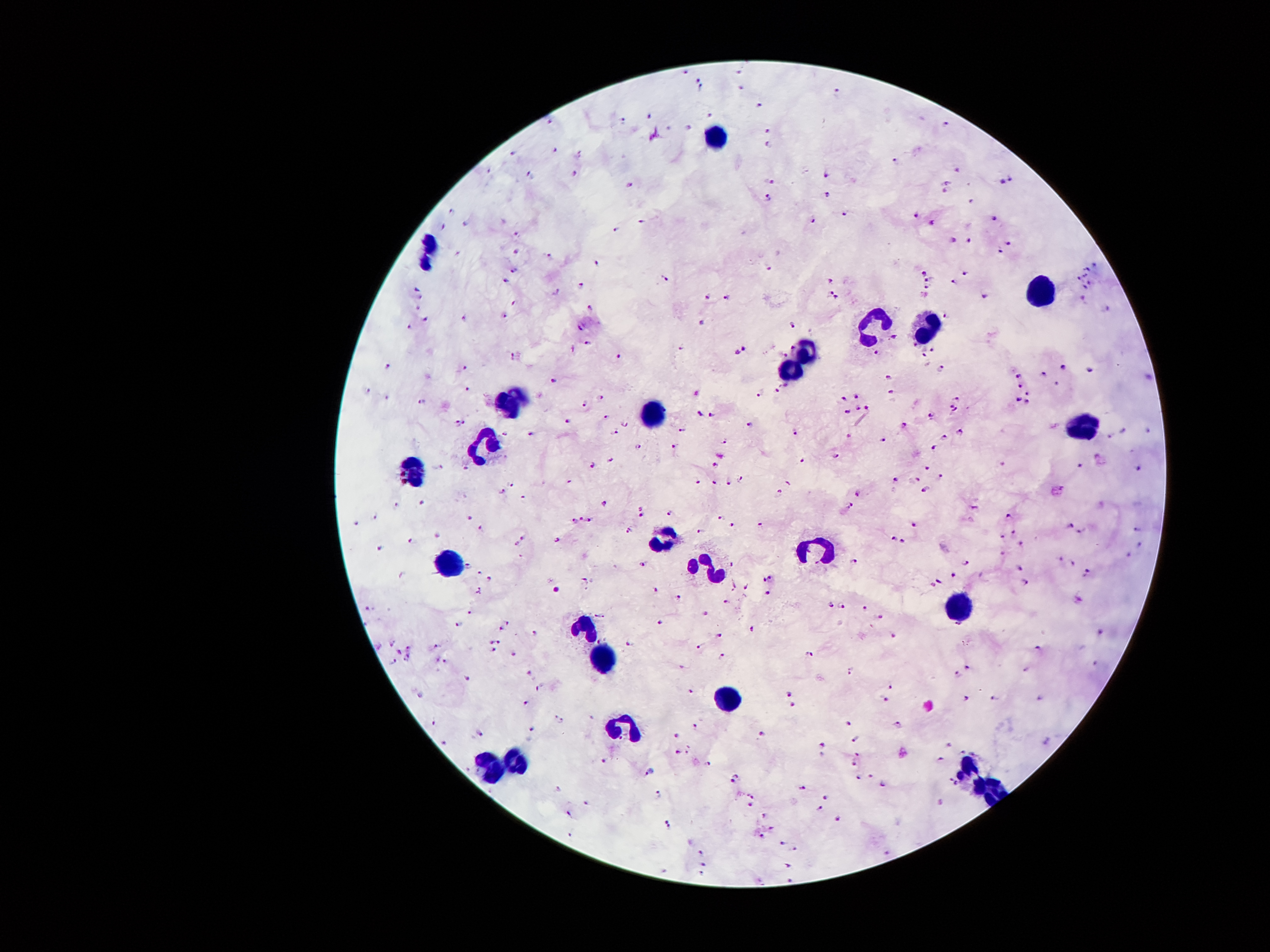

{
  "stain": "Giemsa",
  "leukocyte_locations": "approximate object centers, in pixels from the top-left corner: (x=714, y=135), (x=425, y=253), (x=1038, y=293), (x=870, y=328), (x=928, y=329), (x=801, y=356), (x=788, y=369), (x=509, y=402), (x=649, y=414), (x=1088, y=427), (x=486, y=446), (x=414, y=471), (x=666, y=545), (x=807, y=551), (x=448, y=566), (x=708, y=571), (x=956, y=610), (x=586, y=625), (x=605, y=659), (x=731, y=699), (x=628, y=726), (x=511, y=764), (x=486, y=766), (x=966, y=766), (x=989, y=793)",
  "image_size": "1270×952 pixels",
  "preparation": "thick blood smear",
  "field_of_view": "single",
  "magnification": "100x",
  "plasmodium_parasite_locations": "approximate object centers, in pixels from the top-left corner: (x=686, y=73), (x=739, y=73), (x=698, y=78), (x=701, y=89), (x=741, y=89), (x=835, y=93), (x=757, y=105), (x=708, y=113), (x=649, y=118), (x=550, y=122), (x=621, y=123), (x=945, y=125), (x=688, y=129), (x=767, y=131), (x=770, y=146), (x=556, y=150), (x=514, y=154), (x=579, y=155), (x=897, y=162), (x=574, y=174), (x=826, y=174), (x=531, y=175), (x=1009, y=178), (x=1002, y=181), (x=768, y=182), (x=946, y=182), (x=629, y=185), (x=946, y=192), (x=827, y=195), (x=769, y=199), (x=971, y=200), (x=451, y=212), (x=844, y=213), (x=917, y=213), (x=994, y=218), (x=814, y=221), (x=641, y=222), (x=465, y=223), (x=933, y=224), (x=443, y=227), (x=617, y=229), (x=516, y=235), (x=953, y=240), (x=968, y=242), (x=1009, y=243), (x=999, y=250), (x=517, y=253), (x=457, y=254), (x=548, y=257), (x=598, y=264), (x=1093, y=266), (x=767, y=268), (x=1086, y=270), (x=513, y=272), (x=923, y=273), (x=963, y=273), (x=1085, y=277), (x=664, y=278), (x=833, y=278), (x=1078, y=279), (x=506, y=280), (x=926, y=280), (x=953, y=282), (x=580, y=284), (x=1088, y=284), (x=928, y=287), (x=1083, y=288), (x=554, y=292), (x=829, y=293), (x=987, y=293), (x=707, y=296), (x=420, y=297), (x=836, y=297), (x=1083, y=297), (x=726, y=298), (x=510, y=303), (x=590, y=307), (x=417, y=308), (x=1105, y=310), (x=945, y=314), (x=503, y=316), (x=424, y=317), (x=465, y=319), (x=701, y=322), (x=794, y=324), (x=581, y=326), (x=408, y=327), (x=896, y=336), (x=588, y=343), (x=915, y=347), (x=933, y=348), (x=681, y=349), (x=745, y=350), (x=735, y=352), (x=783, y=353), (x=876, y=353), (x=923, y=354), (x=621, y=356), (x=516, y=357), (x=1065, y=367), (x=389, y=368), (x=464, y=369), (x=941, y=369), (x=1090, y=370), (x=1044, y=374), (x=886, y=375), (x=1018, y=375), (x=552, y=382), (x=1055, y=383), (x=787, y=385), (x=1020, y=385), (x=369, y=390), (x=467, y=390), (x=697, y=391), (x=777, y=391), (x=892, y=392), (x=1026, y=392), (x=856, y=395), (x=759, y=396), (x=603, y=398), (x=844, y=399), (x=955, y=399), (x=1019, y=400), (x=1027, y=401), (x=420, y=403), (x=584, y=403), (x=857, y=407), (x=867, y=408), (x=953, y=408), (x=848, y=411), (x=698, y=413), (x=711, y=414), (x=932, y=417), (x=605, y=418), (x=568, y=422), (x=460, y=423), (x=626, y=425), (x=904, y=425), (x=748, y=426), (x=684, y=427), (x=1148, y=430), (x=1124, y=431), (x=793, y=432), (x=958, y=432), (x=615, y=433), (x=504, y=434), (x=529, y=435), (x=1110, y=435), (x=851, y=436), (x=944, y=438), (x=723, y=441), (x=883, y=442), (x=639, y=446), (x=674, y=446), (x=935, y=448), (x=834, y=456), (x=612, y=461), (x=803, y=461), (x=593, y=466), (x=1078, y=467), (x=714, y=468), (x=926, y=468), (x=465, y=469), (x=1137, y=469), (x=942, y=476), (x=896, y=478), (x=740, y=479), (x=915, y=479), (x=569, y=482), (x=789, y=482), (x=698, y=484), (x=729, y=484), (x=513, y=485), (x=712, y=485), (x=925, y=490), (x=502, y=491), (x=778, y=492), (x=856, y=493), (x=523, y=498), (x=424, y=504), (x=605, y=505), (x=642, y=506), (x=397, y=507), (x=850, y=508), (x=974, y=508), (x=670, y=514), (x=642, y=516), (x=1009, y=516), (x=375, y=518), (x=469, y=518), (x=718, y=518), (x=575, y=520), (x=581, y=520), (x=589, y=521), (x=356, y=523), (x=914, y=524), (x=731, y=525), (x=759, y=526), (x=1070, y=526), (x=481, y=528), (x=1012, y=529), (x=628, y=530), (x=1136, y=530), (x=699, y=531), (x=1080, y=531), (x=1001, y=534), (x=438, y=536), (x=893, y=537), (x=523, y=538), (x=559, y=540), (x=412, y=541), (x=903, y=541), (x=1022, y=544), (x=517, y=545), (x=1139, y=545), (x=378, y=547), (x=1001, y=554), (x=1129, y=555), (x=1060, y=559), (x=965, y=561), (x=853, y=564), (x=730, y=565), (x=1073, y=565), (x=466, y=566), (x=644, y=566), (x=1019, y=570), (x=1088, y=573), (x=480, y=574), (x=954, y=575), (x=491, y=578), (x=768, y=578), (x=583, y=581), (x=940, y=581), (x=1026, y=584), (x=731, y=587), (x=746, y=588), (x=479, y=591), (x=659, y=591), (x=768, y=593), (x=680, y=599), (x=1080, y=599), (x=724, y=603), (x=829, y=604), (x=841, y=606), (x=369, y=609), (x=866, y=610), (x=704, y=612), (x=471, y=614), (x=600, y=615), (x=882, y=617), (x=506, y=623), (x=662, y=624), (x=458, y=625), (x=755, y=627), (x=501, y=629), (x=536, y=634), (x=724, y=634), (x=1100, y=634), (x=892, y=636), (x=395, y=642), (x=490, y=642), (x=498, y=643), (x=436, y=644), (x=629, y=644), (x=699, y=645), (x=378, y=646), (x=410, y=648), (x=493, y=650), (x=1038, y=650), (x=399, y=652), (x=513, y=654), (x=724, y=654), (x=811, y=654), (x=407, y=660), (x=446, y=660), (x=392, y=663), (x=1095, y=665), (x=682, y=668), (x=967, y=668), (x=1026, y=669), (x=851, y=671), (x=530, y=673), (x=956, y=674), (x=465, y=676), (x=891, y=687), (x=538, y=690), (x=690, y=693), (x=788, y=694), (x=422, y=695), (x=992, y=698), (x=1039, y=698), (x=882, y=699), (x=964, y=699), (x=524, y=702), (x=793, y=706), (x=592, y=717), (x=558, y=720), (x=845, y=723), (x=434, y=724), (x=898, y=726), (x=531, y=729), (x=695, y=729), (x=480, y=735), (x=764, y=735), (x=677, y=736), (x=853, y=738), (x=447, y=743), (x=822, y=745), (x=949, y=745), (x=689, y=749), (x=677, y=754), (x=856, y=755), (x=604, y=758), (x=940, y=759), (x=709, y=762), (x=853, y=763), (x=649, y=770), (x=856, y=777), (x=868, y=777), (x=735, y=779), (x=883, y=784), (x=555, y=788), (x=801, y=788), (x=659, y=793), (x=751, y=794), (x=825, y=798), (x=588, y=802), (x=749, y=805), (x=820, y=808), (x=569, y=815), (x=767, y=815), (x=836, y=819), (x=667, y=824), (x=772, y=827), (x=761, y=835), (x=781, y=842), (x=796, y=848), (x=702, y=851), (x=704, y=864), (x=787, y=867), (x=702, y=874)",
  "patient_malaria_status": "infected with Plasmodium falciparum",
  "capture": "smartphone through the microscope eyepiece"
}